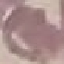

Summary:
  - Malaria status: uninfected
  - Capture: smartphone through the microscope eyepiece
  - Stain: Giemsa
  - Image type: cell patch, automatically extracted from a larger field of view and resized to 64 × 64 pixels
  - Preparation: thin smear